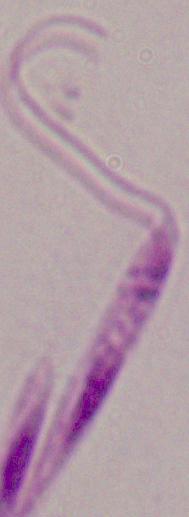

A Leishmania parasite is shown. Photomicrograph. Captured at 1000x magnification.